Assess for malaria.
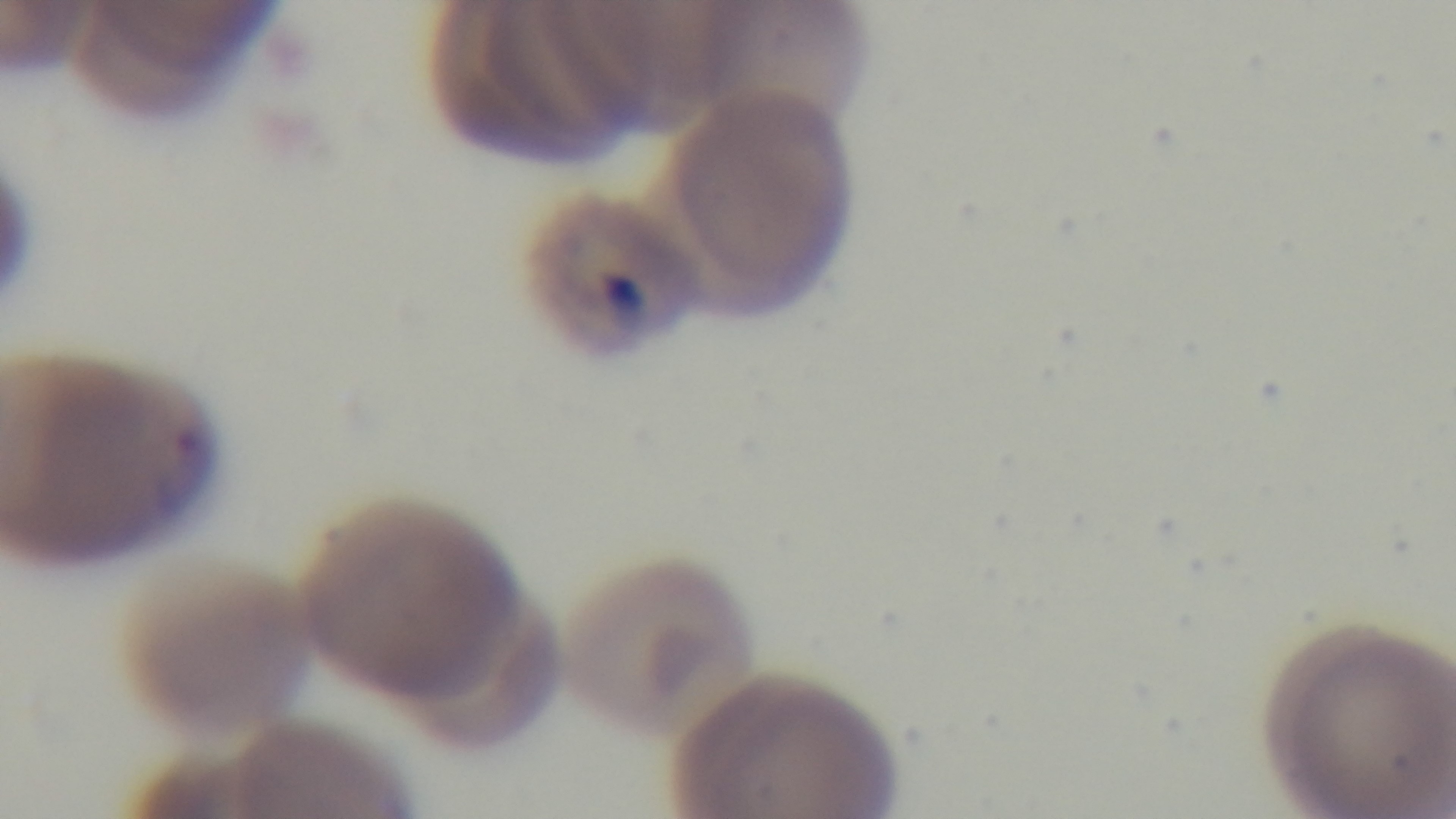
It is infected.

Photomicrograph. Preparation: thin blood film. Giemsa stain. Oil-immersion objective, 100x. Mounted 4K digital camera. Single field of view.